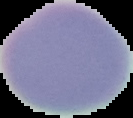

result = no malaria parasites seen
image size = 133×118 pixels
image type = cell region segmented out of the field of view; surrounding area masked to black
preparation = thin blood film